Assess this cell for malaria.
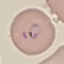

Parasitized.

Thin blood film. Acquired by smartphone through the microscope eyepiece. Automatically extracted cell patch, resized to 64 × 64 pixels. Giemsa-stained preparation.